Assess this cell for malaria.
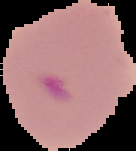

It is parasitized.

From a thin blood film. Image is 136×151 pixels. The area outside the segmented cell region is set to black.